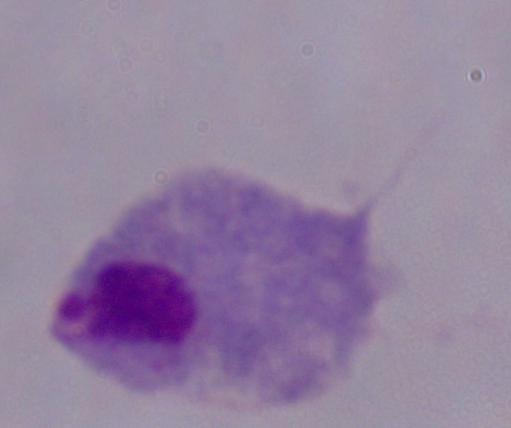

{
  "magnification": "1000x",
  "identification": "trichomonad",
  "modality": "photomicrograph"
}